Classify this cell by malaria status.
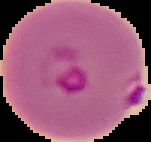

It is parasitized.

The area outside the segmented cell region is set to black. From a thin blood film. Image is 151×142 pixels.